State which cell type is depicted.
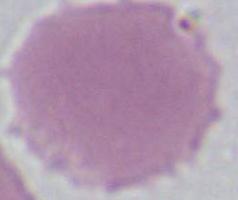

This is an erythrocyte.

Micrograph. 1000x magnification.